Name the parasite shown.
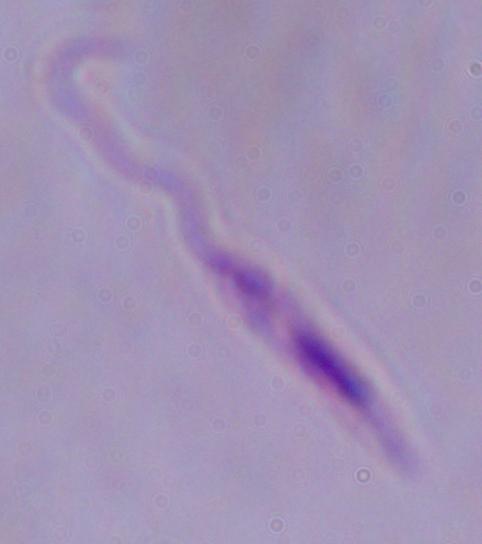

Leishmania.

1000x magnification. Photomicrograph.